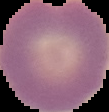
Summary:
  - Image size: 109×112 pixels
  - Image type: cell region segmented out of the field of view; surrounding area masked to black
  - Result: no Plasmodium parasites detected
  - Preparation: thin blood smear